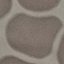
Result: negative for malaria parasites. Giemsa-stained preparation. Thin blood film. Automatically extracted cell patch, resized to 64 × 64 pixels. Acquired by smartphone through the microscope eyepiece.